Give the extent of all Plasmodium falciparum-infected red blood cells.
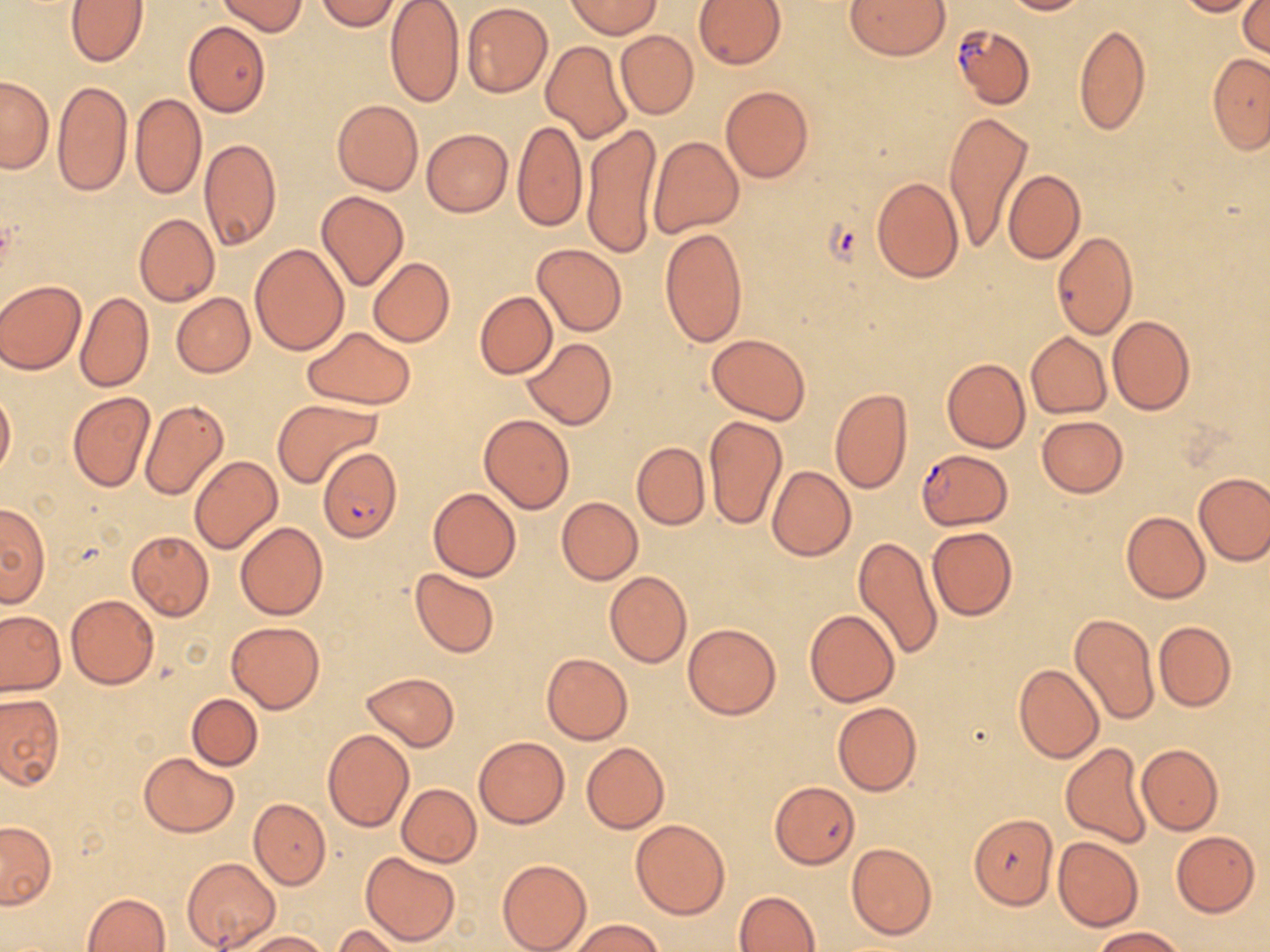
Approximate bounding boxes as (x1,y1)-(x2,y2) corner pairs in pixels.
Plasmodium falciparum-infected red blood cells: (951,23)-(1034,110), (320,449)-(403,543), (916,449)-(1012,529).

Summary:
  - Uninfected red blood cell locations: (315,0)-(401,30), (846,0)-(950,58), (1000,0)-(1086,15), (1174,0)-(1260,17), (65,1)-(148,66), (218,1)-(307,35), (384,1)-(464,107), (567,1)-(662,38), (694,1)-(786,70), (462,2)-(553,98), (1238,2)-(1269,55), (184,22)-(271,116), (1074,23)-(1151,136), (615,30)-(699,120), (541,41)-(631,143), (1207,53)-(1270,152), (0,75)-(54,174), (53,81)-(132,197), (721,85)-(813,183), (130,95)-(207,199), (331,100)-(423,195), (944,109)-(1034,253), (512,121)-(587,233), (582,122)-(663,258), (421,129)-(512,217), (647,136)-(743,238), (199,139)-(282,249), (1003,170)-(1084,264), (871,178)-(964,281), (317,191)-(408,291), (277,198)-(375,332), (134,213)-(220,306), (660,227)-(747,348), (1051,231)-(1138,339), (250,244)-(350,355), (533,244)-(626,335), (368,258)-(454,345), (0,279)-(86,374), (474,291)-(557,378), (76,292)-(155,392), (172,293)-(254,377), (1107,316)-(1193,415), (304,327)-(416,408), (1026,332)-(1111,418), (707,333)-(810,422), (522,339)-(615,428), (942,358)-(1030,453), (0,385)-(16,478), (830,389)-(912,493), (67,391)-(155,491), (140,399)-(229,501), (274,399)-(380,488), (480,413)-(574,513), (705,415)-(786,529), (1037,416)-(1127,497), (632,443)-(710,529), (189,457)-(281,553), (768,466)-(856,560), (1195,472)-(1270,564), (428,488)-(520,580), (557,497)-(643,584), (0,502)-(50,607), (1121,511)-(1210,603), (235,522)-(328,621), (927,527)-(1017,621), (127,530)-(213,621), (853,537)-(943,662), (411,567)-(499,658), (605,572)-(692,667), (66,593)-(159,689), (804,610)-(900,706), (0,611)-(65,695), (1070,614)-(1159,725), (227,621)-(324,713), (1154,621)-(1235,710), (684,623)-(781,720), (542,653)-(632,743), (1013,664)-(1103,763), (362,672)-(458,751), (165,693)-(255,825), (187,693)-(262,770), (0,694)-(64,788), (832,702)-(920,796), (322,729)-(414,831), (474,736)-(568,828), (581,742)-(668,833), (1059,743)-(1153,848), (1137,744)-(1222,834), (140,753)-(238,835), (769,781)-(859,869), (397,783)-(481,866), (250,799)-(330,888), (968,812)-(1059,909), (630,818)-(729,919), (0,820)-(56,908), (1170,830)-(1260,918), (1053,836)-(1144,931), (846,842)-(937,942), (361,852)-(460,946), (182,857)-(281,950), (497,858)-(591,952), (735,891)-(820,952), (82,893)-(170,952), (567,917)-(664,951), (331,924)-(407,951), (1092,926)-(1186,951), (239,930)-(332,951)
  - Slide-level diagnosis: Plasmodium falciparum
  - Magnification: 1000x
  - Stain: May-Grünwald-Giemsa
  - Preparation: thin blood film
  - Modality: optical microscopy
  - Image size: 1270×952 pixels
  - Field of view: single